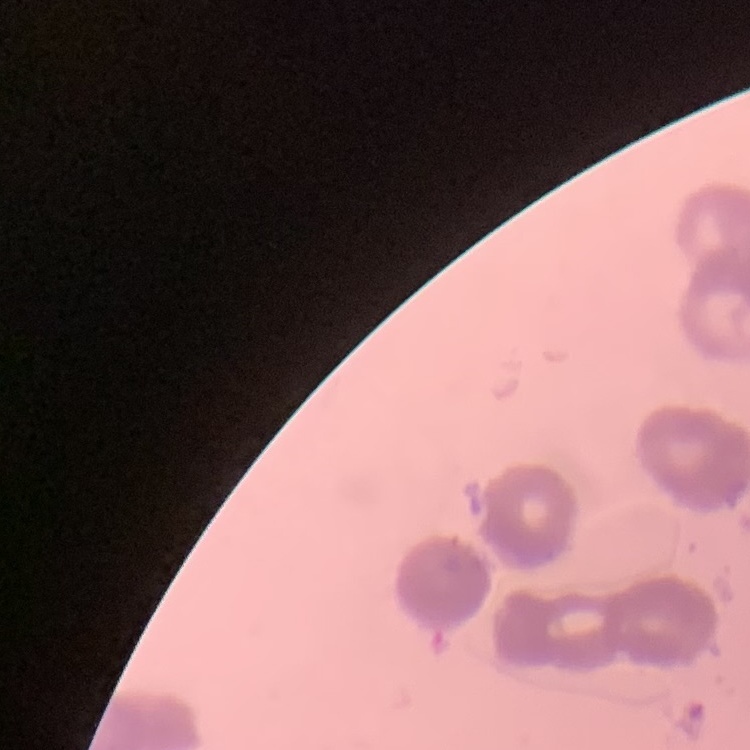
Summary:
  - Erythrocyte morphology: rouleaux formation
  - Preparation: thin blood smear
  - Image type: one tile cut from a larger photomicrograph
  - Stain: Field's or Giemsa